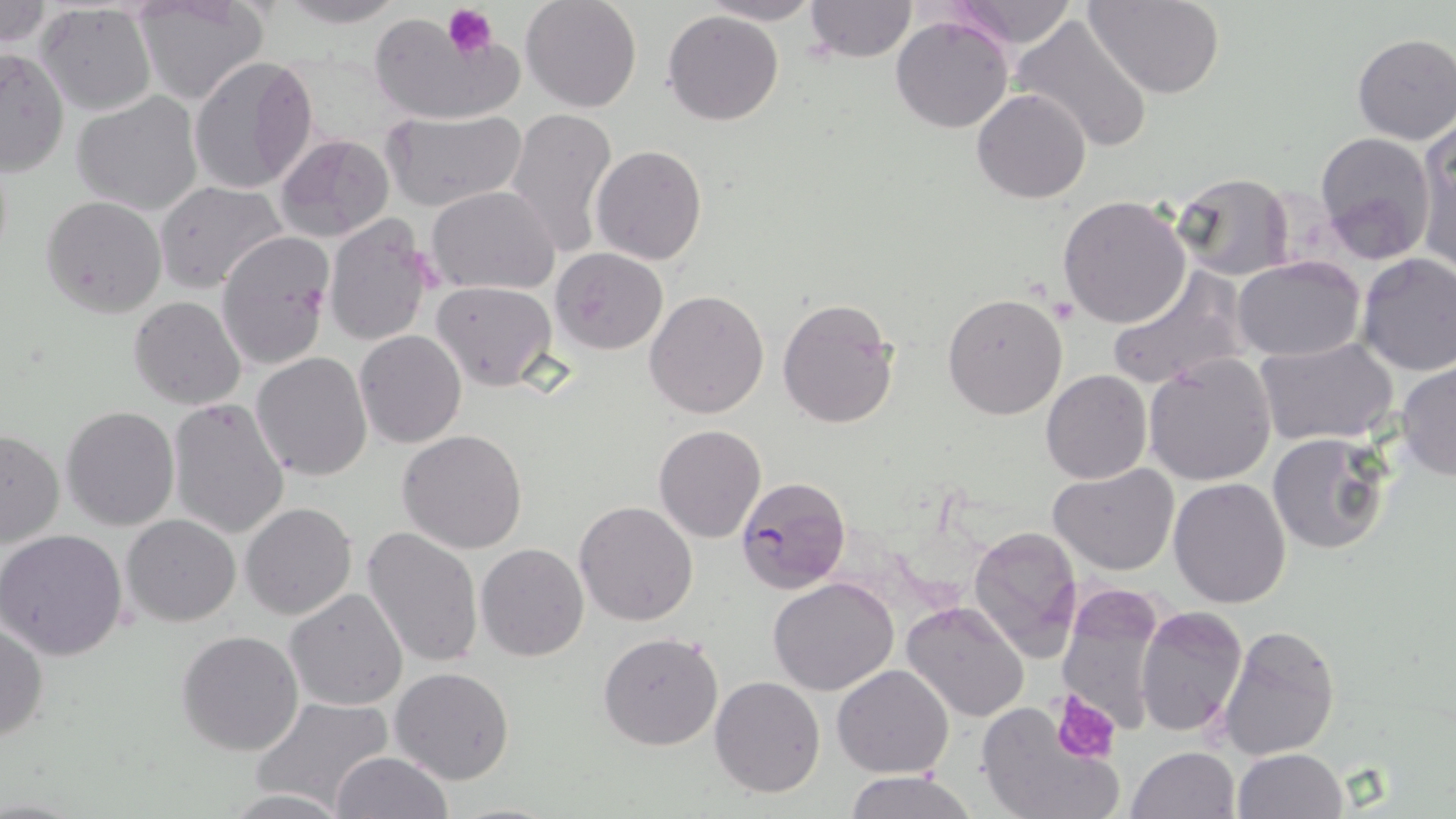

Plasmodium falciparum-infected red blood cell locations = approximate bounding boxes as (x1,y1)-(x2,y2) corner pairs in pixels: (734,474)-(851,594)
slide-level diagnosis = Plasmodium falciparum
image size = 1456×819 pixels
modality = light microscopy
stain = May-Grünwald-Giemsa
field of view = single
uninfected red blood cell locations = approximate bounding boxes as (x1,y1)-(x2,y2) corner pairs in pixels: (134,0)-(271,106), (270,0)-(409,28), (520,0)-(642,113), (698,0)-(826,25), (948,0)-(1078,48), (1084,0)-(1225,99), (802,1)-(918,62), (0,2)-(54,49), (34,3)-(158,118), (663,11)-(786,126), (1011,13)-(1154,153), (370,15)-(515,127), (890,15)-(1014,133), (1351,33)-(1456,145), (54,39)-(169,180), (0,48)-(69,175), (188,56)-(318,195), (972,88)-(1091,203), (71,91)-(204,216), (505,107)-(618,259), (384,110)-(527,214), (1416,127)-(1456,275), (1313,131)-(1437,260), (277,133)-(397,239), (591,144)-(707,264), (1168,172)-(1295,280), (157,182)-(290,293), (427,185)-(559,295), (1057,194)-(1192,328), (42,195)-(167,317), (323,214)-(435,347), (216,231)-(335,370), (551,248)-(669,354), (1357,253)-(1455,377), (1233,255)-(1365,362), (1106,268)-(1250,391), (432,281)-(558,390), (644,290)-(770,419), (941,292)-(1068,420), (777,295)-(902,430), (129,296)-(245,408), (354,329)-(466,447), (1255,338)-(1398,448), (251,352)-(374,480), (1143,356)-(1277,486), (1396,362)-(1456,481), (1041,369)-(1151,484), (167,398)-(290,541), (61,407)-(179,530), (653,424)-(766,542), (0,429)-(64,550), (398,430)-(529,553), (1269,432)-(1393,555), (1048,464)-(1179,576), (1169,478)-(1292,607), (574,500)-(699,626), (241,502)-(357,619), (121,514)-(240,627), (967,525)-(1084,659), (362,527)-(484,671), (0,529)-(128,661), (475,543)-(589,662), (767,577)-(898,696), (285,587)-(409,711), (1054,588)-(1167,737), (899,603)-(1030,722), (1134,605)-(1248,738), (0,622)-(49,742), (1219,624)-(1341,760), (177,629)-(304,756), (598,632)-(723,751), (833,664)-(954,779), (389,667)-(514,786), (710,676)-(825,798), (250,697)-(395,811), (974,703)-(1123,819), (1125,746)-(1239,819), (1232,748)-(1347,819), (331,750)-(451,819), (844,771)-(977,819), (222,789)-(352,818)
magnification = 1000x
preparation = thin blood film
platelet locations = approximate bounding boxes as (x1,y1)-(x2,y2) corner pairs in pixels: (443,2)-(499,59), (1050,692)-(1120,764)